Report the malaria status of this cell.
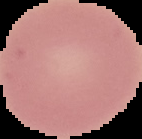

It is uninfected.

Segmented cell region on a black background. Image is 142×139 pixels. From a thin blood film.